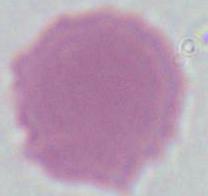
Summary:
  - Modality: photomicrograph
  - Magnification: 1000x
  - Identification: red blood cell